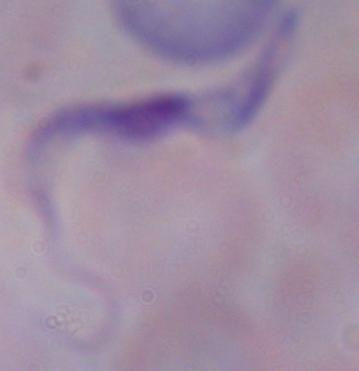

identification = trypanosome
magnification = 1000x
modality = photomicrograph